Assess the morphology of the red blood cells.
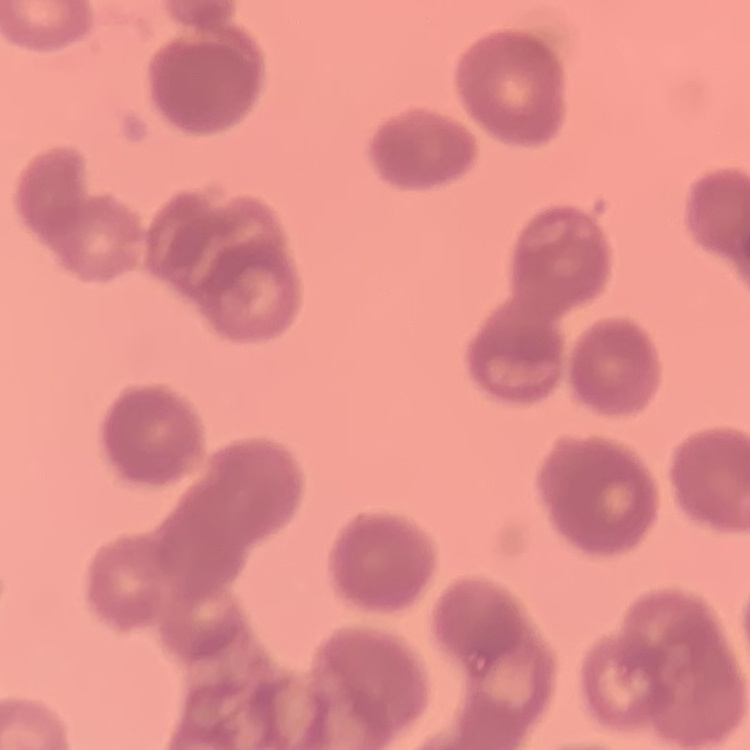
Rouleaux formation.

Thin peripheral smear. Stained with either Field's or Giemsa. Square crop of a larger photomicrograph.